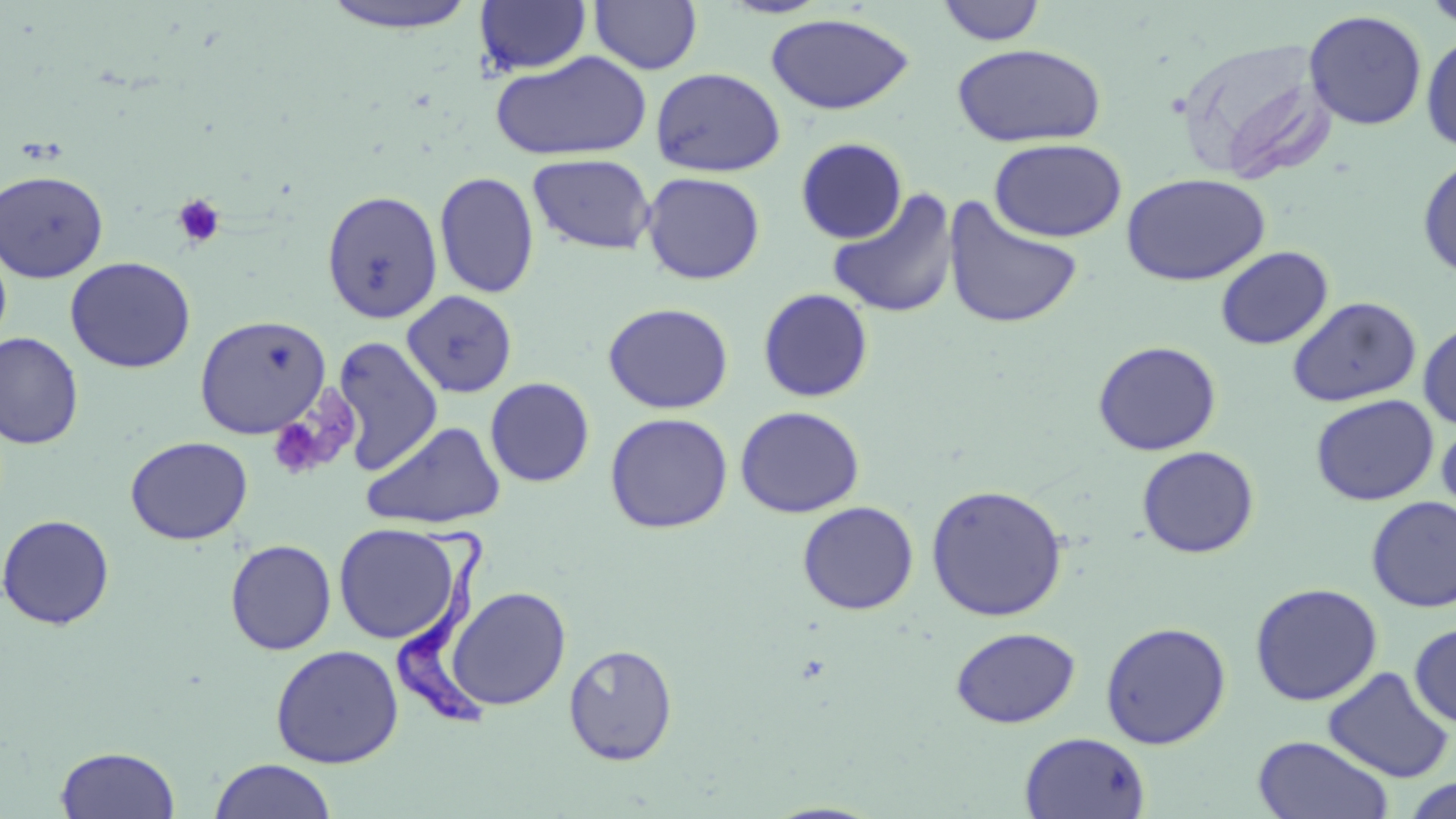
Approximate bounding boxes as (x1,y1)-(x2,y2) corner pairs in pixels. Uninfected red blood cell locations: (589,0)-(702,75), (717,0)-(836,19), (1421,0)-(1456,32), (317,1)-(483,34), (475,1)-(591,76), (936,1)-(1046,46), (1303,9)-(1428,131), (765,13)-(915,115), (1420,32)-(1456,154), (1177,37)-(1336,185), (952,43)-(1107,148), (490,50)-(653,162), (650,67)-(786,177), (795,137)-(907,244), (989,138)-(1127,242), (527,153)-(657,255), (1417,154)-(1456,280), (0,170)-(109,282), (434,171)-(540,299), (641,171)-(765,285), (1121,172)-(1271,286), (827,187)-(960,320), (321,190)-(443,324), (943,196)-(1085,331), (0,236)-(12,352), (1215,246)-(1334,350), (64,256)-(196,373), (758,287)-(874,402), (401,290)-(518,398), (1287,296)-(1422,407), (602,302)-(734,414), (194,314)-(332,439), (1418,319)-(1456,431), (0,332)-(84,450), (331,336)-(443,476), (1093,340)-(1222,456), (485,377)-(595,487), (1310,394)-(1439,506), (735,405)-(865,518), (604,412)-(733,533), (1436,419)-(1456,525), (361,420)-(506,529), (125,436)-(253,545), (1137,445)-(1259,558), (926,483)-(1067,621), (1366,497)-(1456,613), (797,501)-(919,615), (0,513)-(116,630), (333,523)-(464,645), (225,539)-(336,655), (1249,582)-(1383,706), (447,586)-(571,710), (1100,621)-(1232,749), (1409,622)-(1456,728), (950,627)-(1081,728), (563,643)-(679,765), (270,644)-(404,768), (1322,667)-(1454,783), (1019,731)-(1151,819), (1252,735)-(1394,819), (54,745)-(181,818), (208,758)-(336,819), (1400,775)-(1456,818). Platelet locations: (172,194)-(226,249), (267,388)-(358,482). Trypanosoma brucei locations: (396,521)-(495,730). Slide-level diagnosis: Trypanosoma brucei. One field of a larger specimen. Image is 1456×819 pixels. Thin blood smear. Captured at 1000x magnification. May-Grünwald-Giemsa stain. Light microscopy.